State which parasite is depicted.
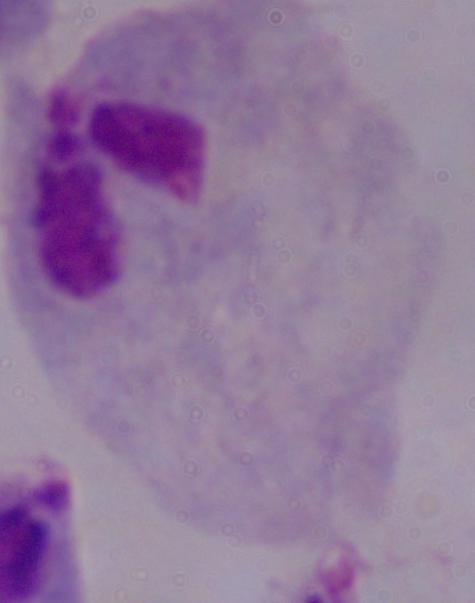
A trichomonad.

Summary:
  - Magnification: 1000x
  - Modality: micrograph